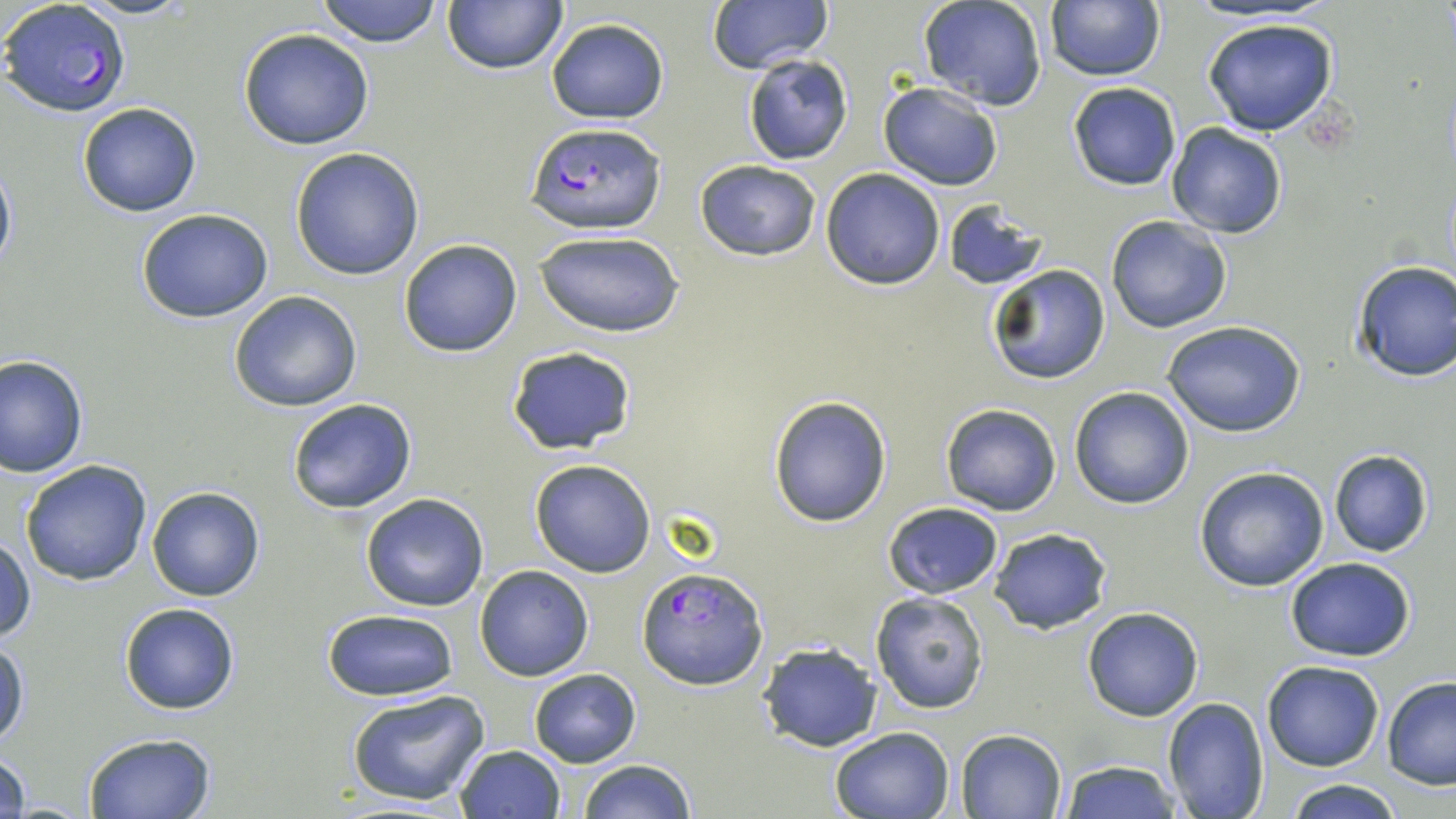

Summary:
  - Coordinate format: approximate bounding boxes as [x1, y1, x2, y2] in pixels
  - Uninfected red blood cell locations: [79, 0, 196, 20], [316, 0, 443, 47], [443, 0, 565, 73], [706, 0, 833, 73], [917, 2, 1048, 110], [1045, 2, 1165, 82], [545, 18, 668, 123], [1201, 18, 1343, 137], [239, 28, 374, 150], [743, 55, 852, 166], [876, 81, 1004, 190], [1067, 81, 1181, 191], [77, 101, 202, 217], [1166, 123, 1286, 238], [290, 148, 425, 280], [0, 155, 16, 279], [696, 160, 819, 262], [820, 168, 945, 290], [944, 199, 1048, 293], [135, 207, 274, 323], [1106, 215, 1232, 333], [535, 231, 685, 338], [399, 238, 522, 357], [1348, 260, 1456, 383], [984, 264, 1112, 385], [229, 291, 362, 411], [1163, 319, 1307, 438], [505, 346, 637, 455], [1, 355, 88, 476], [1068, 386, 1196, 511], [768, 395, 892, 526], [286, 398, 418, 515], [939, 403, 1063, 516], [1328, 449, 1433, 558], [21, 459, 153, 586], [530, 459, 656, 577], [1194, 466, 1330, 593], [146, 486, 265, 601], [360, 493, 488, 611], [881, 501, 1003, 600], [987, 527, 1111, 633], [0, 531, 36, 645], [1284, 555, 1417, 660], [476, 565, 594, 681], [871, 591, 992, 714], [118, 603, 240, 715], [1081, 606, 1203, 720], [321, 609, 459, 702], [0, 635, 30, 748], [758, 643, 883, 752], [1261, 660, 1385, 770], [528, 667, 641, 768], [1381, 676, 1456, 790], [348, 689, 491, 806], [1161, 697, 1269, 819], [829, 727, 954, 818], [955, 728, 1067, 818], [83, 731, 217, 818], [454, 745, 566, 819], [0, 748, 32, 819], [575, 758, 696, 819], [1058, 760, 1184, 818], [1282, 778, 1407, 819]
  - Plasmodium falciparum-infected red blood cell locations: [2, 0, 132, 116], [526, 122, 664, 235], [636, 568, 767, 688]
  - Slide-level diagnosis: Plasmodium falciparum
  - Preparation: thin blood film
  - Modality: optical microscopy
  - Stain: May-Grünwald-Giemsa
  - Field of view: one of a larger specimen
  - Image size: 1456×819 pixels
  - Magnification: 1000x